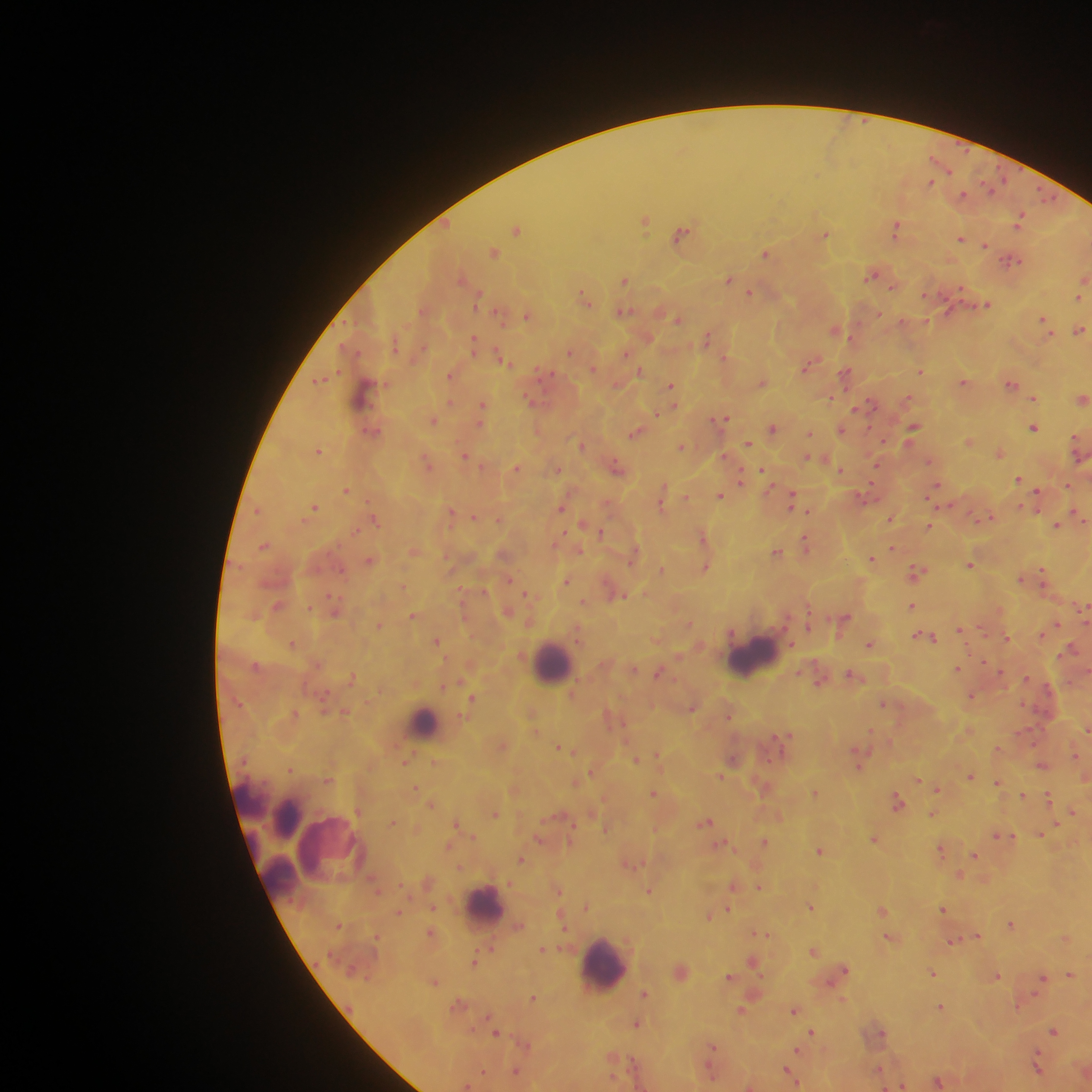 Approximate centers as x y in pixels. Malaria parasite locations: 929 183; 990 187; 962 194; 1047 198; 1020 220; 645 222; 517 228; 895 228; 682 233; 825 235; 961 239; 985 245; 493 252; 765 253; 1010 261; 871 274; 728 279; 626 280; 893 287; 750 293; 584 296; 478 297; 1078 297; 985 304; 623 311; 527 315; 676 318; 1044 322; 1079 330; 835 331; 707 338; 474 343; 570 352; 626 353; 501 358; 807 365; 594 369; 921 370; 640 371; 846 372; 450 376; 320 379; 762 382; 964 382; 1011 383; 671 387; 363 393; 830 398; 1034 398; 1082 399; 864 405; 483 407; 857 408; 723 418; 434 421; 913 428; 1034 428; 772 429; 841 430; 372 432; 635 433; 809 433; 969 442; 1076 443; 748 444; 581 445; 682 446; 319 450; 999 453; 465 455; 807 457; 929 461; 427 463; 616 466; 517 468; 840 469; 764 471; 742 476; 1018 479; 935 487; 346 490; 663 492; 721 496; 1037 496; 792 500; 662 502; 314 507; 562 507; 451 512; 1078 514; 474 517; 890 518; 987 518; 499 519; 1082 519; 375 520; 1058 524; 928 525; 601 532; 702 537; 805 542; 264 546; 579 550; 776 552; 634 553; 872 558; 370 561; 970 565; 706 567; 661 569; 916 572; 1043 575; 1021 578; 566 580; 1045 583; 619 594; 913 606; 1083 610; 412 616; 845 619; 689 622; 809 622; 1056 624; 380 625; 961 629; 927 637; 1006 637; 436 640; 293 644; 869 645; 1073 647; 634 669; 958 669; 659 673; 852 675; 819 680; 971 696; 472 698; 882 703; 692 707; 345 711; 729 714; 1086 727; 783 738; 559 747; 1076 754; 657 755; 733 759; 405 760; 635 760; 858 764; 1042 765; 289 769; 970 776; 721 777; 327 779; 919 780; 998 783; 416 787; 936 789; 654 793; 815 793; 1023 795; 1048 798; 898 802; 1072 811; 933 813; 495 814; 706 822; 1041 834; 1002 836; 873 839; 764 842; 720 845; 820 850; 942 851; 974 855; 521 859; 959 876; 733 886; 759 887; 649 890; 586 907; 810 907; 729 908; 942 909; 882 910; 398 912; 708 916; 1011 924; 762 933; 976 936; 889 938; 952 941; 543 949; 814 950; 474 960; 753 961; 844 970; 933 973; 1070 975; 996 976; 729 977; 1041 979; 434 982; 644 994; 533 998; 458 1003; 941 1006; 793 1010; 741 1011; 637 1024; 1054 1031; 811 1032; 877 1032; 496 1033; 712 1046; 795 1052; 1037 1066; 483 1071; 516 1071; 788 1071; 880 1071; 938 1082; 901 1085. Leukocyte locations: 752 657; 553 661; 424 722; 247 798; 286 814; 333 851; 277 879; 485 903; 602 963. Sample from Ghana. Thick blood film. Photographed through a microscope with a mobile-phone camera. Image is 1092×1092 pixels. One field of view.